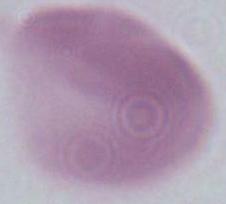
{
  "magnification": "1000x",
  "modality": "photomicrograph",
  "identification": "erythrocyte"
}